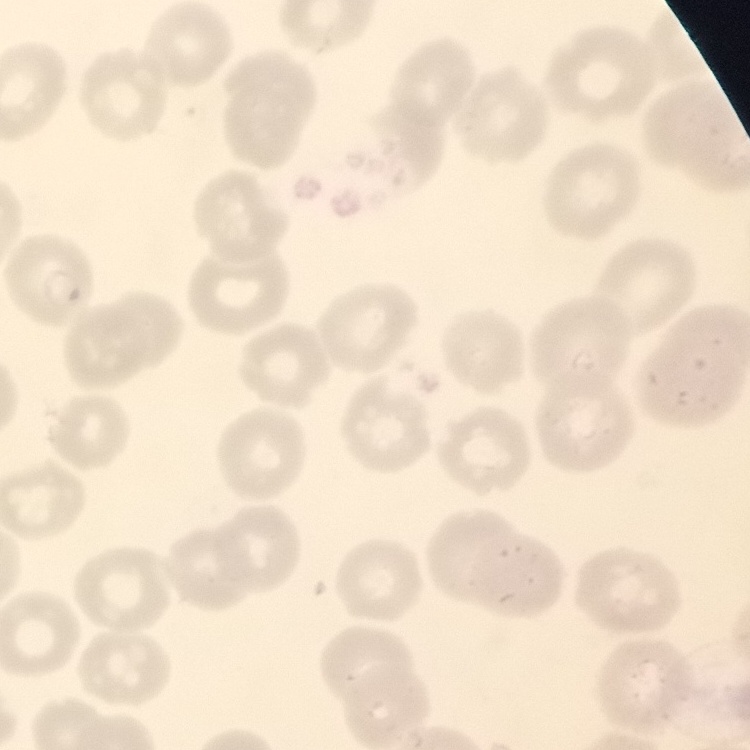

The red blood cells exhibit no rouleaux formation. Stained with either Field's or Giemsa. One tile cut from a larger photomicrograph. Thin blood smear.